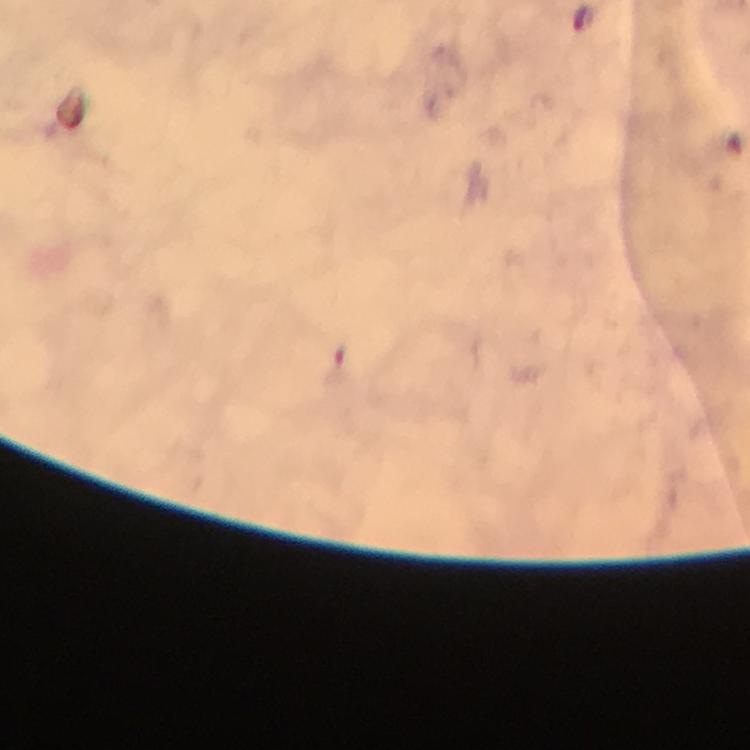
Approximate centers as {x, y} in pixels.
Summary:
  - Malaria parasite locations: {582, 16}
  - Context: from a diagnostic examination for malaria
  - Magnification: 100x
  - Cropped from: a single field of view
  - Capture: smartphone photograph through a microscope
  - Preparation: thick blood smear
  - Immersion oil: used
  - Stain: Giemsa
  - Image size: 750×750 pixels